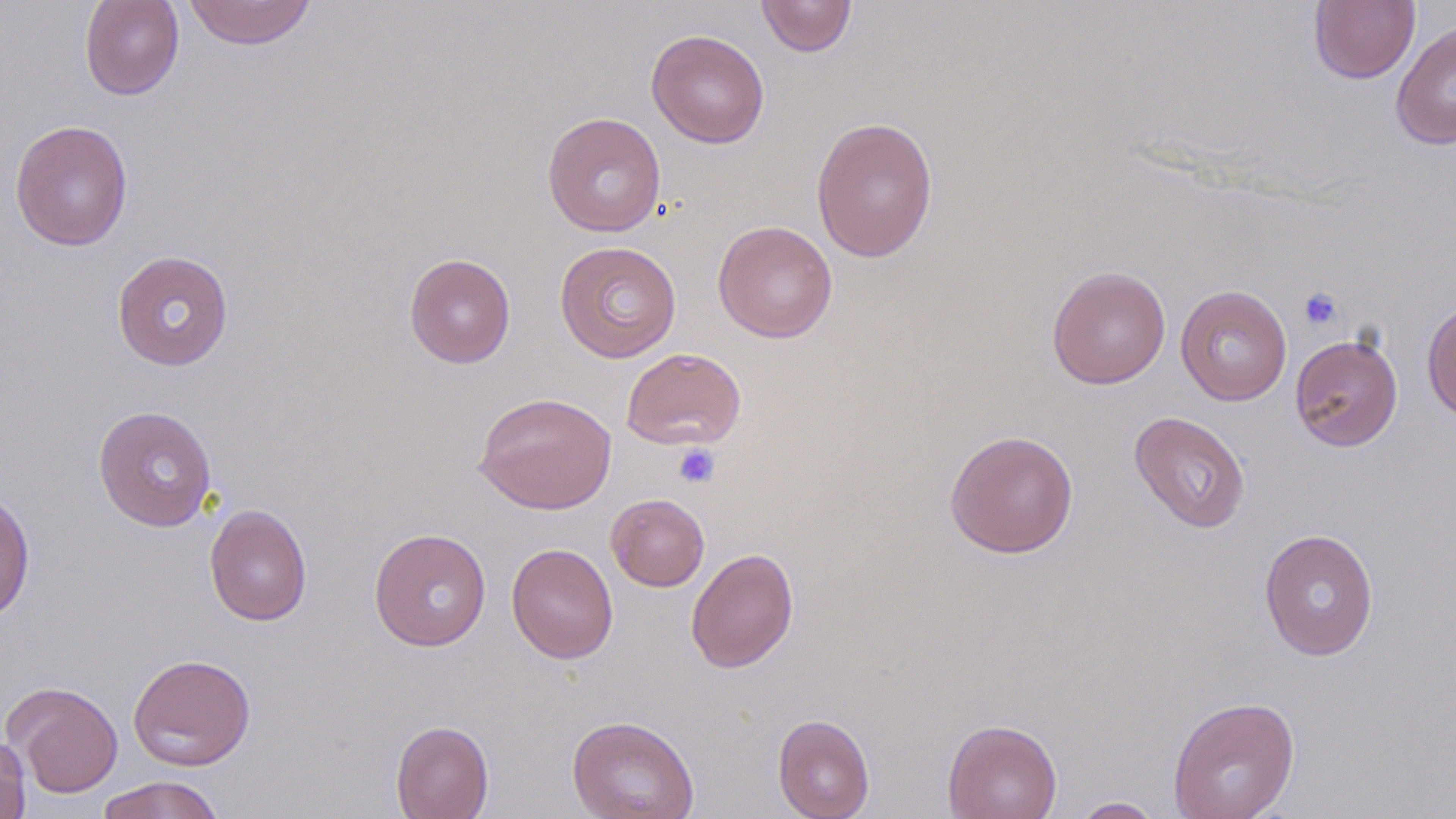 Approximate bounding boxes as (x1,y1)-(x2,y2) corner pairs in pixels. Platelet locations: (1298,287)-(1342,331), (673,443)-(720,488). Uninfected red blood cell locations: (79,0)-(185,101), (182,0)-(317,49), (756,0)-(857,57), (1308,1)-(1420,84), (1390,21)-(1456,151), (646,29)-(770,148), (542,112)-(666,237), (811,116)-(939,263), (9,119)-(133,251), (713,220)-(838,343), (555,240)-(681,363), (111,250)-(234,370), (404,252)-(516,368), (1046,265)-(1171,389), (1175,285)-(1292,406), (1422,300)-(1456,423), (1289,333)-(1403,451), (621,347)-(747,450), (473,392)-(617,515), (93,405)-(217,531), (1129,411)-(1251,533), (944,429)-(1079,558), (0,488)-(36,622), (606,493)-(709,591), (204,503)-(313,626), (369,528)-(491,651), (1259,528)-(1379,661), (506,542)-(619,663), (686,548)-(799,673), (127,653)-(256,770), (3,681)-(123,797), (1167,695)-(1301,819), (772,713)-(875,819), (566,715)-(700,819), (942,718)-(1062,819), (390,720)-(494,819), (0,732)-(31,819), (96,775)-(226,819), (1070,796)-(1165,818). Slide-level diagnosis: negative for blood parasites. May-Grünwald-Giemsa stain. Thin blood smear. Optical microscopy. One field of a larger specimen. Captured at 1000x magnification. Image is 1456×819 pixels.